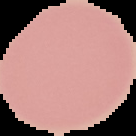
malaria status = uninfected
image size = 136×136 pixels
preparation = thin blood smear
image type = cell region segmented out of the field of view; surrounding area masked to black